Give the preparation type.
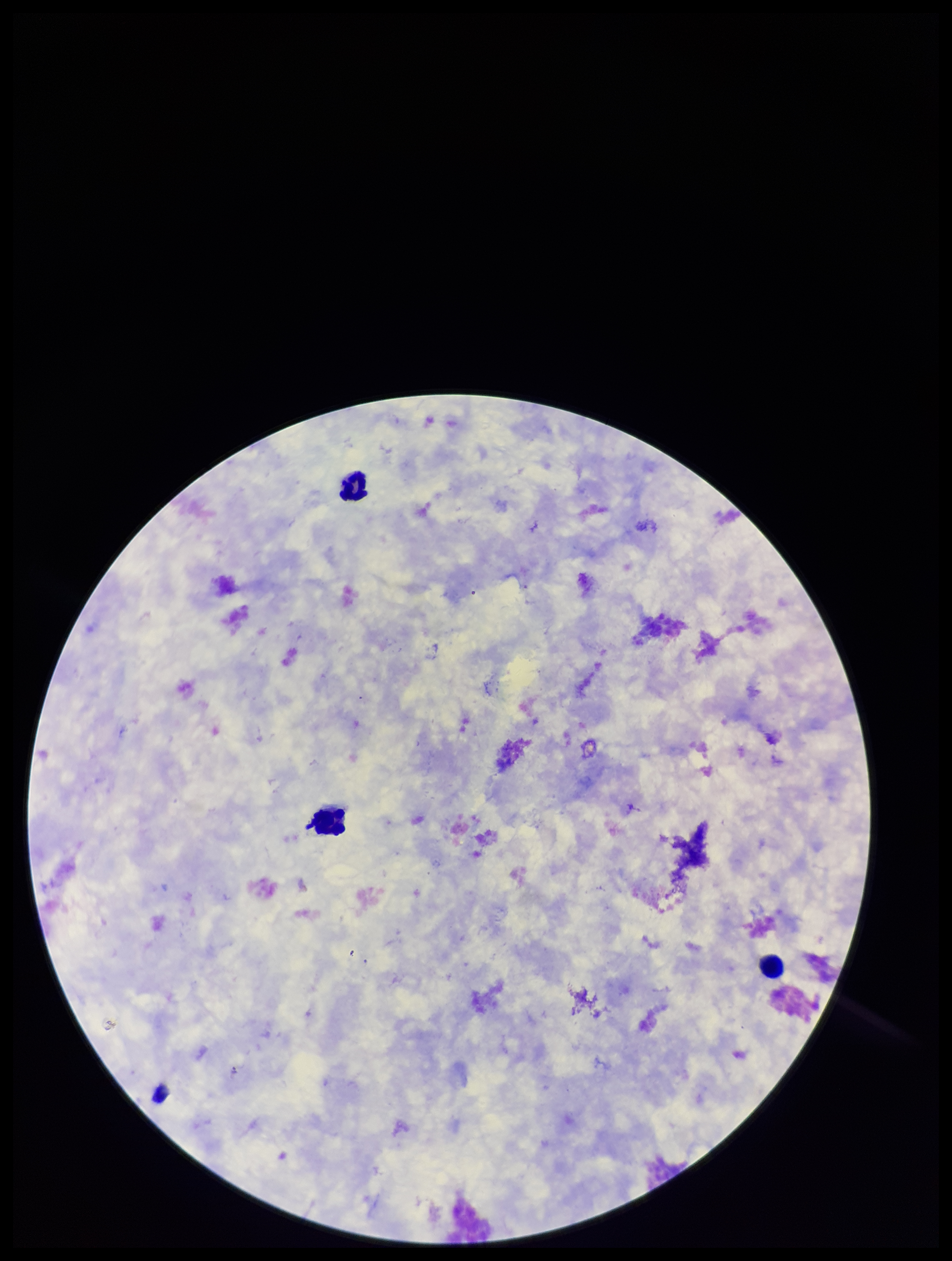

It is a thick blood smear.

Summary:
  - Field of view: one from this slide
  - Image size: 952×1261 pixels
  - Parasite count: 0
  - Patient malaria status: negative
  - Stain: Giemsa
  - Leukocyte count: 3
  - Plasmodium parasites: none identified
  - Capture: smartphone photograph through the microscope eyepiece